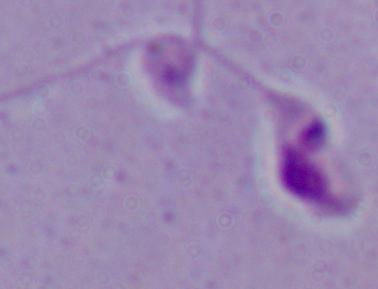
{
  "magnification": "1000x",
  "modality": "photomicrograph",
  "identification": "Leishmania"
}